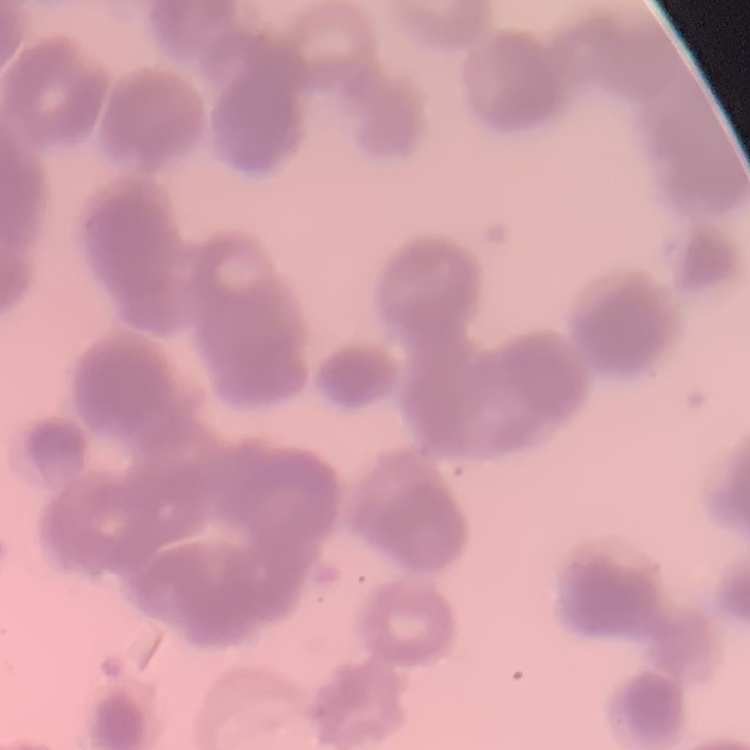

red blood cell morphology = rouleaux formation
image type = square crop of a larger photomicrograph
preparation = thin peripheral smear
stain = Field's or Giemsa